Report the malaria status of this cell.
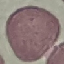
It is uninfected.

Summary:
  - Stain: Giemsa
  - Image type: automatically extracted cell patch, resized to 64 × 64 pixels
  - Preparation: thin blood film
  - Capture: smartphone through the microscope eyepiece